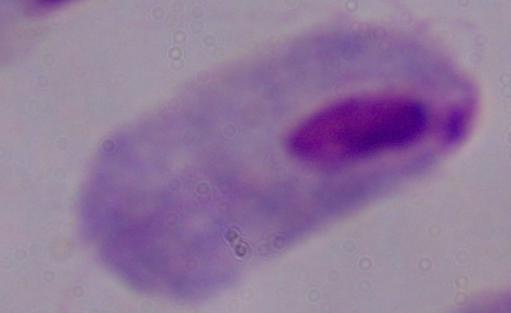
A trichomonad is seen. Micrograph. 1000x magnification.